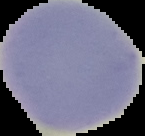

{
  "image_size": "145×136 pixels",
  "preparation": "thin blood film",
  "malaria_status": "uninfected",
  "image_type": "cell region segmented out of the field of view; surrounding area masked to black"
}